Describe the morphology of the erythrocytes.
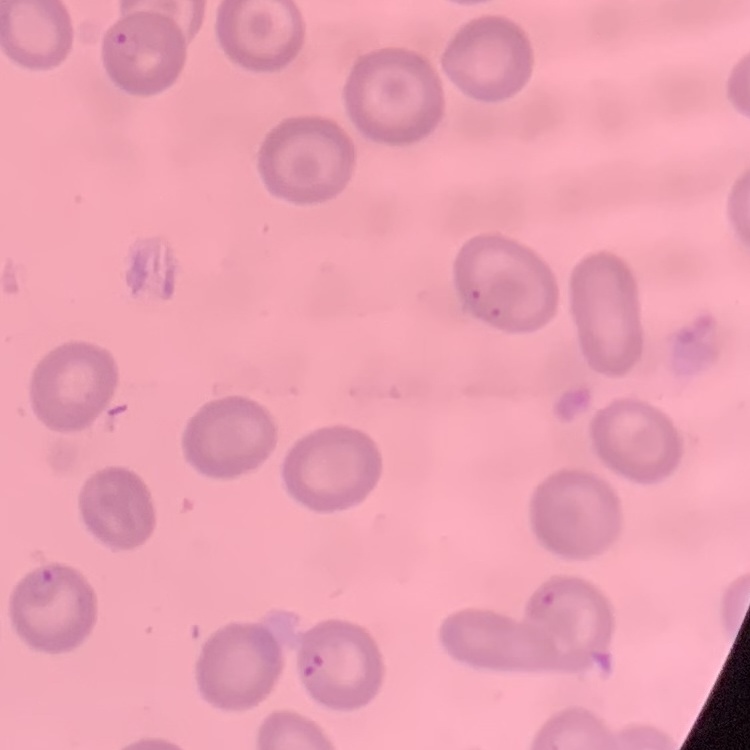
They show no rouleaux formation.

image type = square crop of a larger photomicrograph
stain = Field's or Giemsa
preparation = thin peripheral smear